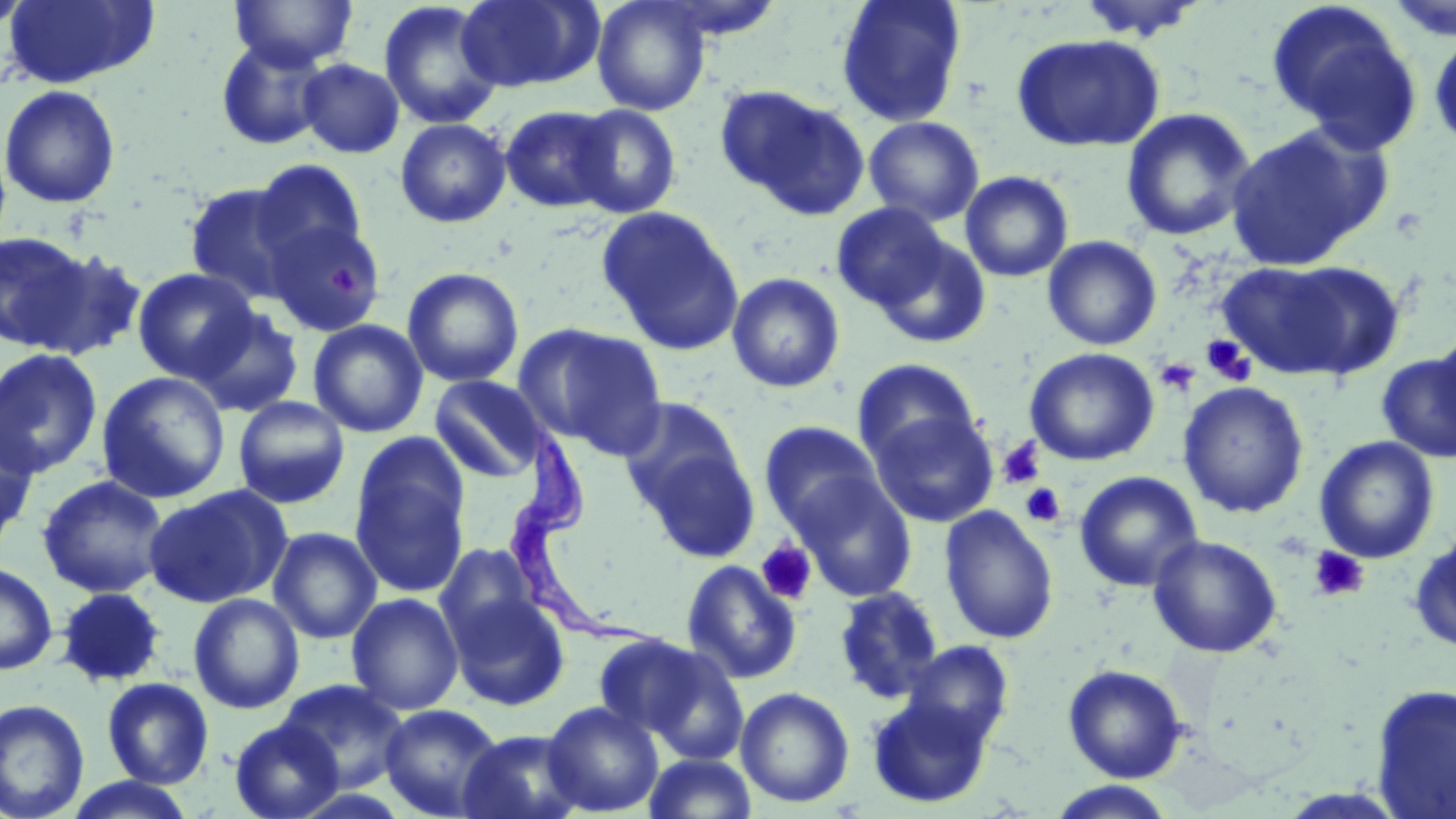

Summary:
  - Coordinate format: approximate bounding boxes as (x1,y1)-(x2,y2) corner pairs in pixels
  - Platelet locations: (328,264)-(358,298), (1201,335)-(1255,386), (1154,357)-(1201,396), (998,437)-(1045,488), (1020,483)-(1065,528), (756,540)-(817,605), (1307,546)-(1370,603)
  - Trypanosoma brucei locations: (505,426)-(673,651)
  - Uninfected red blood cell locations: (1,0)-(32,34), (2,0)-(159,89), (230,0)-(358,70), (456,0)-(602,93), (592,0)-(711,115), (836,0)-(967,127), (1073,0)-(1209,43), (1387,0)-(1456,42), (378,1)-(504,130), (651,1)-(789,44), (1266,1)-(1422,149), (1428,30)-(1456,151), (1010,33)-(1166,153), (216,36)-(332,150), (297,58)-(405,158), (0,84)-(121,209), (717,85)-(870,220), (570,104)-(681,218), (500,105)-(617,212), (1120,107)-(1257,241), (864,116)-(984,226), (395,118)-(511,228), (1224,122)-(1390,270), (250,158)-(369,272), (960,171)-(1074,282), (184,182)-(304,304), (831,202)-(952,312), (597,206)-(745,355), (262,217)-(387,336), (0,229)-(96,352), (870,234)-(991,349), (1043,235)-(1162,351), (30,246)-(148,361), (1219,259)-(1400,383), (132,267)-(259,383), (402,267)-(524,388), (726,272)-(846,393), (188,305)-(304,416), (308,319)-(429,438), (513,323)-(668,458), (1433,326)-(1456,441), (0,347)-(103,480), (1024,347)-(1160,467), (1377,353)-(1456,463), (852,358)-(980,468), (96,371)-(231,504), (429,375)-(546,483), (1177,381)-(1310,519), (232,396)-(351,509), (618,397)-(746,519), (870,409)-(997,527), (0,414)-(39,547), (759,421)-(884,534), (1314,436)-(1440,564), (636,442)-(762,565), (351,446)-(470,596), (1074,471)-(1203,592), (37,474)-(170,598), (791,474)-(917,601), (143,485)-(292,609), (939,505)-(1058,644), (268,527)-(382,644), (1409,529)-(1456,653), (1147,534)-(1283,658), (434,544)-(539,652), (681,560)-(801,685), (0,561)-(58,675), (834,586)-(945,704), (55,587)-(167,688), (447,591)-(571,711), (188,593)-(305,715), (346,593)-(464,715), (596,634)-(745,758), (901,640)-(1014,749), (1063,664)-(1187,782), (102,677)-(214,788), (277,679)-(410,792), (1371,685)-(1456,818), (735,686)-(855,808), (867,693)-(994,809), (0,698)-(90,819), (543,701)-(664,816), (379,703)-(504,818), (230,719)-(344,819), (457,728)-(587,819), (642,752)-(758,819), (61,776)-(199,818), (1046,781)-(1178,819)
  - Slide-level diagnosis: Trypanosoma brucei
  - Image size: 1456×819 pixels
  - Field of view: one of a larger specimen
  - Preparation: thin blood smear
  - Modality: optical microscopy
  - Magnification: 1000x
  - Stain: May-Grünwald-Giemsa